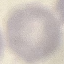

result = no malaria parasites seen
image type = automatically extracted cell patch, resized to 64 × 64 pixels
stain = Giemsa
capture = smartphone through the microscope eyepiece
preparation = thin blood film